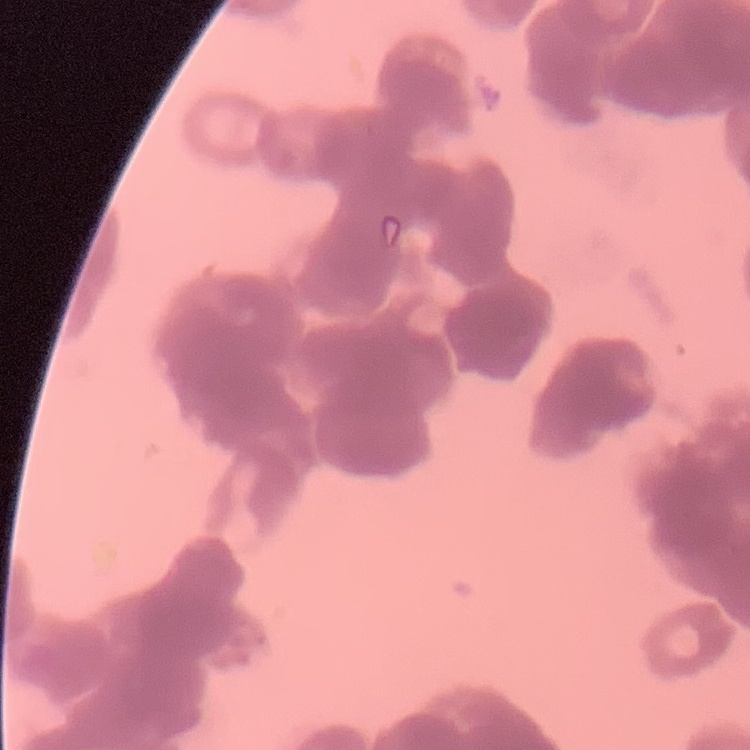 The erythrocytes show rouleaux formation. Stained with either Field's or Giemsa. Thin blood smear. One tile cut from a larger photomicrograph.